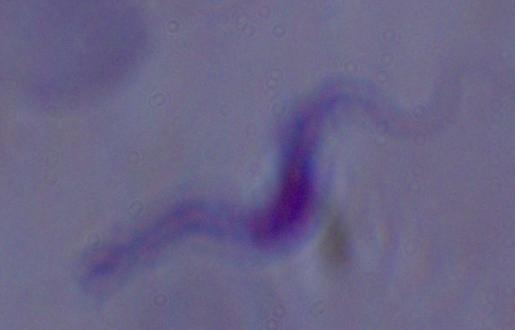

Summary:
  - Identification: trypanosome
  - Magnification: 1000x
  - Modality: micrograph